Classify this cell by malaria status.
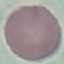
It is uninfected.

Photographed with a smartphone camera at the microscope eyepiece. Cell patch, automatically extracted from a larger field of view and resized to 64 × 64 pixels. Giemsa stain. Thin blood film.